Point out every Plasmodium parasite.
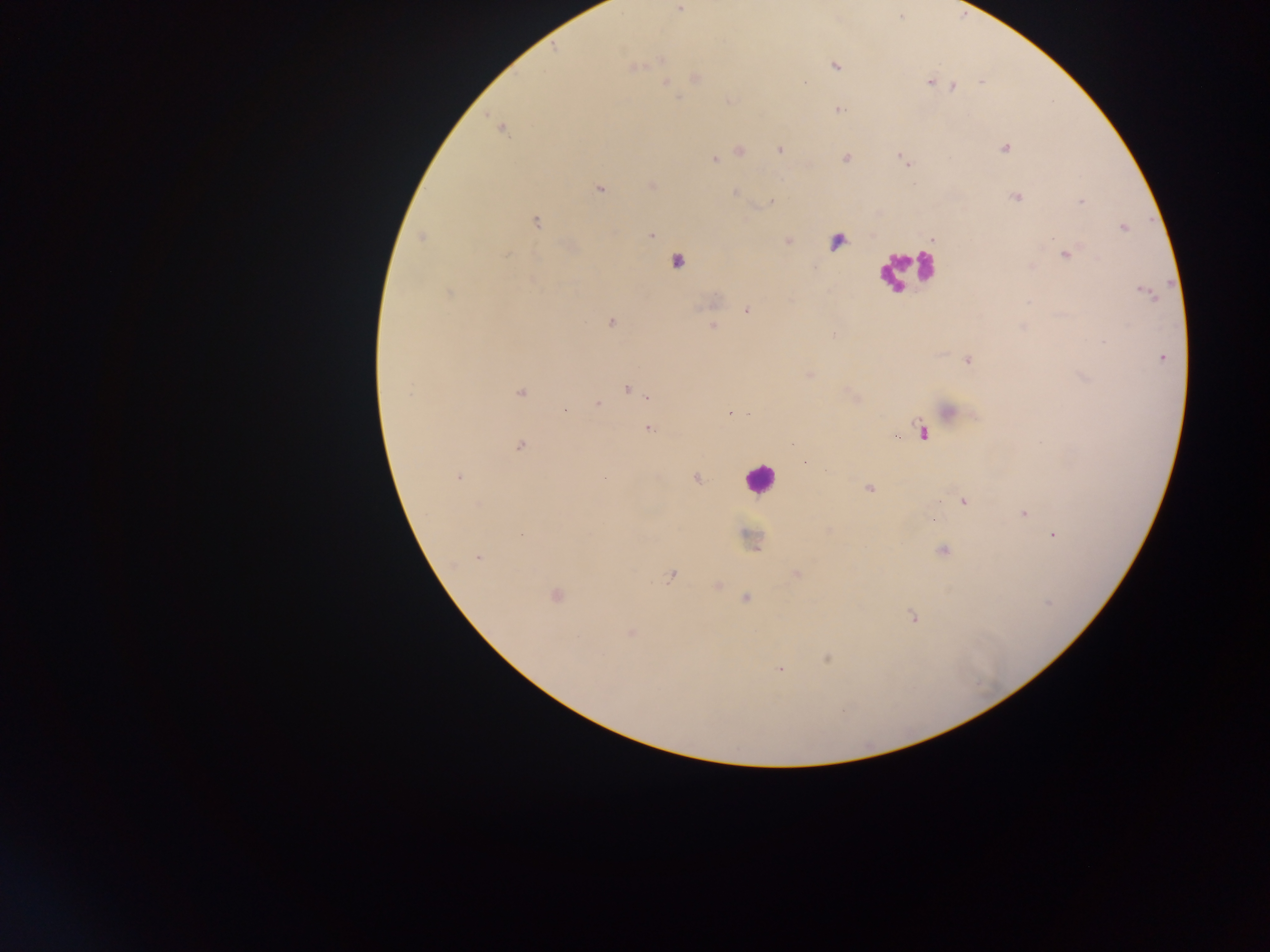

Approximate centers as x y in pixels.
Plasmodium parasites: 680 9; 661 59; 835 66; 633 68; 695 78; 929 82; 668 83; 936 84; 954 86; 837 109; 501 128; 1005 148; 780 150; 740 151; 845 158; 902 159; 715 160; 600 189; 734 193; 1016 198; 771 201; 1081 201; 536 222; 1123 228; 650 235; 422 238; 507 254; 1066 254; 1146 292; 448 293; 746 311; 611 322; 713 326; 833 334; 1104 342; 1161 357; 968 360; 810 374; 627 389; 520 392; 408 394; 647 396; 597 405; 949 410; 731 413; 747 413; 648 429; 921 431; 520 445; 459 477; 695 478; 869 488; 963 501; 1024 513; 523 534; 1053 535; 942 550; 478 557; 796 575; 672 576; 717 586; 555 595; 746 599; 913 616; 631 634; 827 658; 780 669.

Summary:
  - Leukocyte locations: 837 241; 677 261; 904 269; 758 478
  - Preparation: thick blood film
  - Field of view: single
  - Capture: mobile-phone photograph through a microscope
  - Image size: 1270×952 pixels
  - Country: Ghana